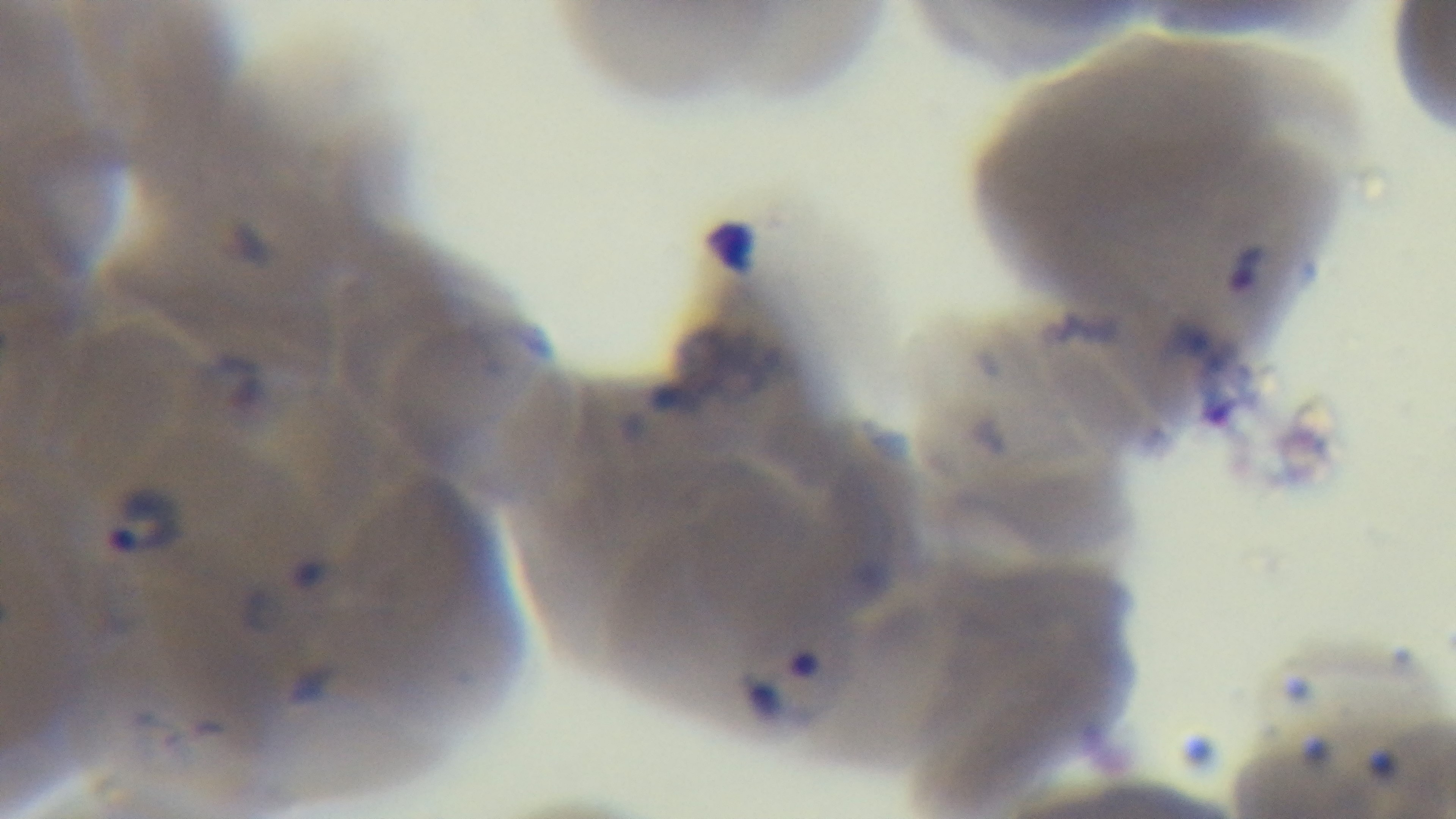

Summary:
  - Modality: light microscopy
  - Objective: 100x oil immersion
  - Stain: Giemsa
  - Capture: mounted 4K digital camera
  - Preparation: thin blood film
  - Field of view: single
  - Malaria status: infected